Report the malaria status of this cell.
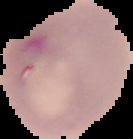
It is parasitized.

image size = 133×139 pixels
image type = segmented cell region on a black background
preparation = thin blood smear